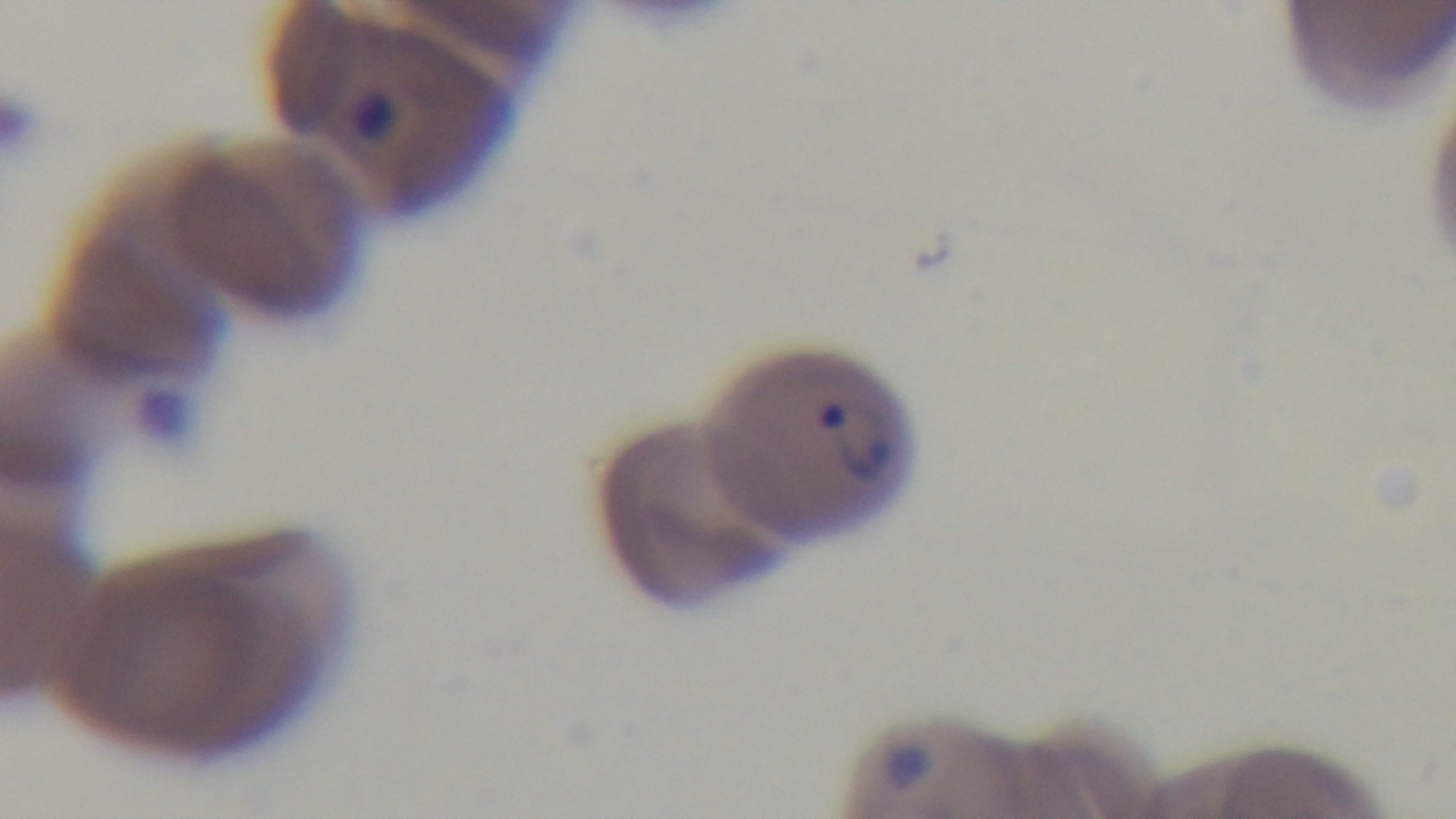
Mounted 4K digital camera. Preparation: thin. Oil-immersion objective, 100x. Single field of view. Giemsa-stained. Malaria status: infected. Light microscopy.